Describe the morphology of the erythrocytes.
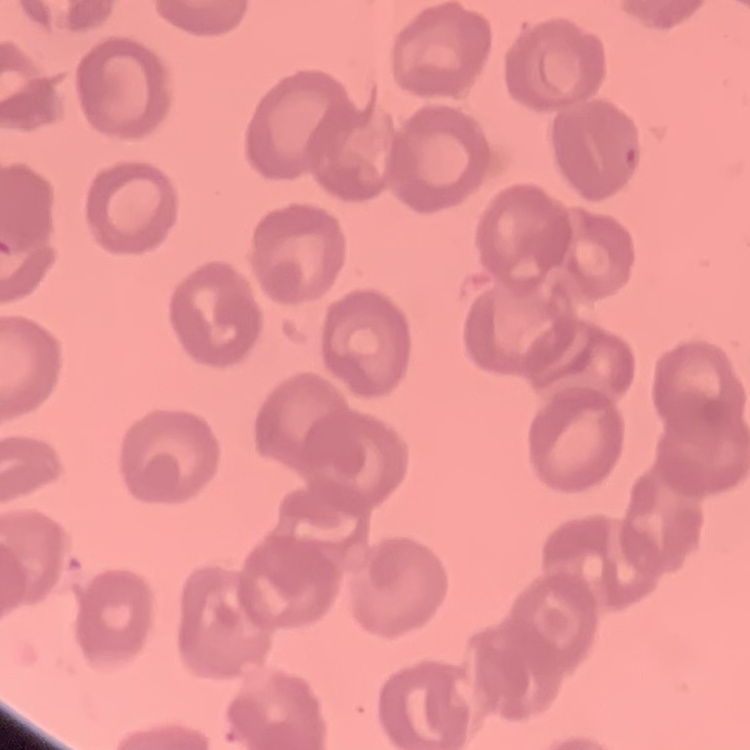
They show no rouleaux formation.

Summary:
  - Stain: Field's or Giemsa
  - Image type: one tile cut from a larger photomicrograph
  - Preparation: thin blood film